Comment on the morphology of the erythrocytes.
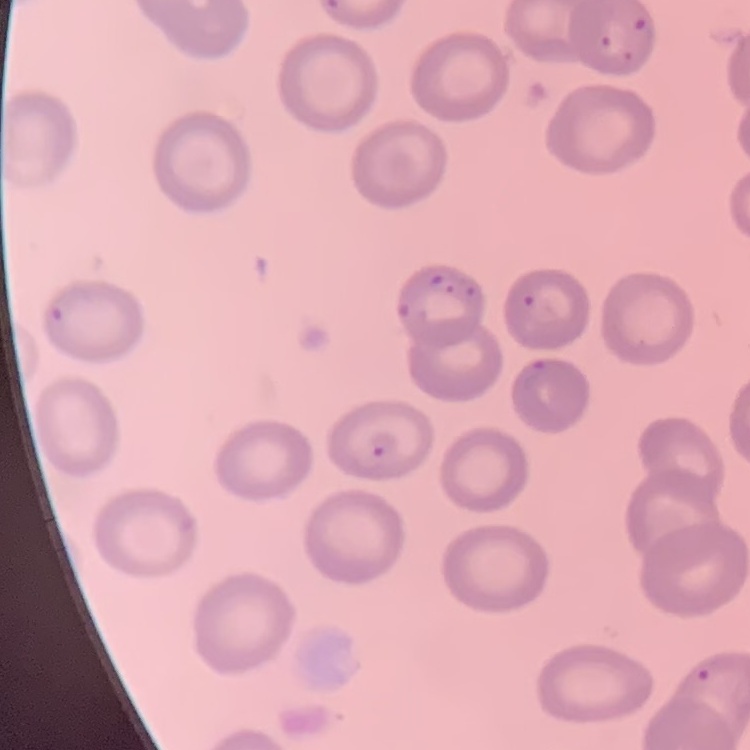

No rouleaux formation.

image_type: one tile cut from a larger photomicrograph
preparation: thin blood film
stain: Field's or Giemsa